Classify this cell by malaria status.
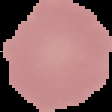

Uninfected.

Summary:
  - Image size: 112×112 pixels
  - Preparation: thin blood smear
  - Image type: segmented cell region on a black background